Assess this cell for malaria.
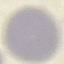
Uninfected.

Thin smear of blood. Automatically extracted cell patch, resized to 64 × 64 pixels. Acquired by smartphone through the microscope eyepiece. Giemsa stain.